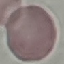

result = no malaria parasites detected
image type = cell patch, automatically extracted from a larger field of view and resized to 64 × 64 pixels
stain = Giemsa
preparation = thin blood smear
capture = smartphone camera at the microscope eyepiece